Assess the morphology of the red blood cells.
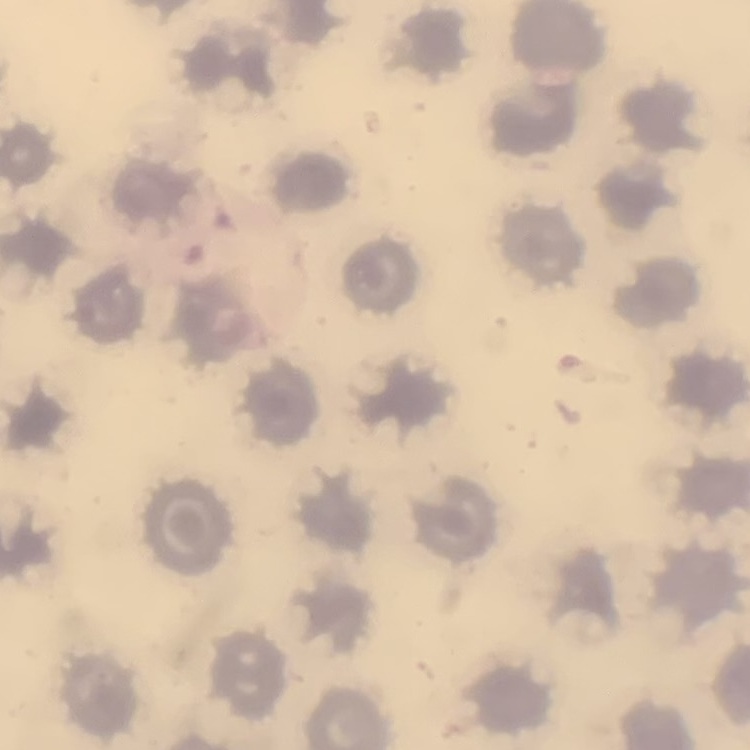

No rouleaux formation.

stain = Field's or Giemsa
image type = square crop of a larger photomicrograph
preparation = thin blood film